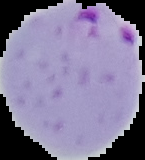
Image is 145×160 pixels. From a thin blood smear. Segmented cell region on a black background. Result: malaria parasites identified.